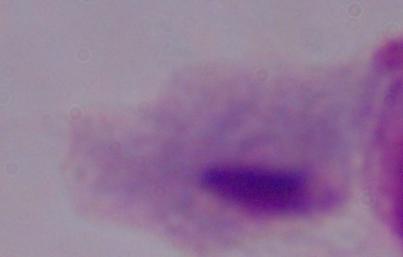

Summary:
  - Modality: micrograph
  - Identification: trichomonad
  - Magnification: 1000x